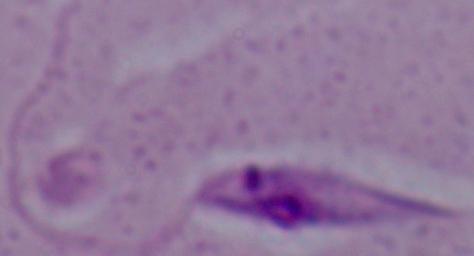
modality: micrograph
magnification: 1000x
identification: Leishmania